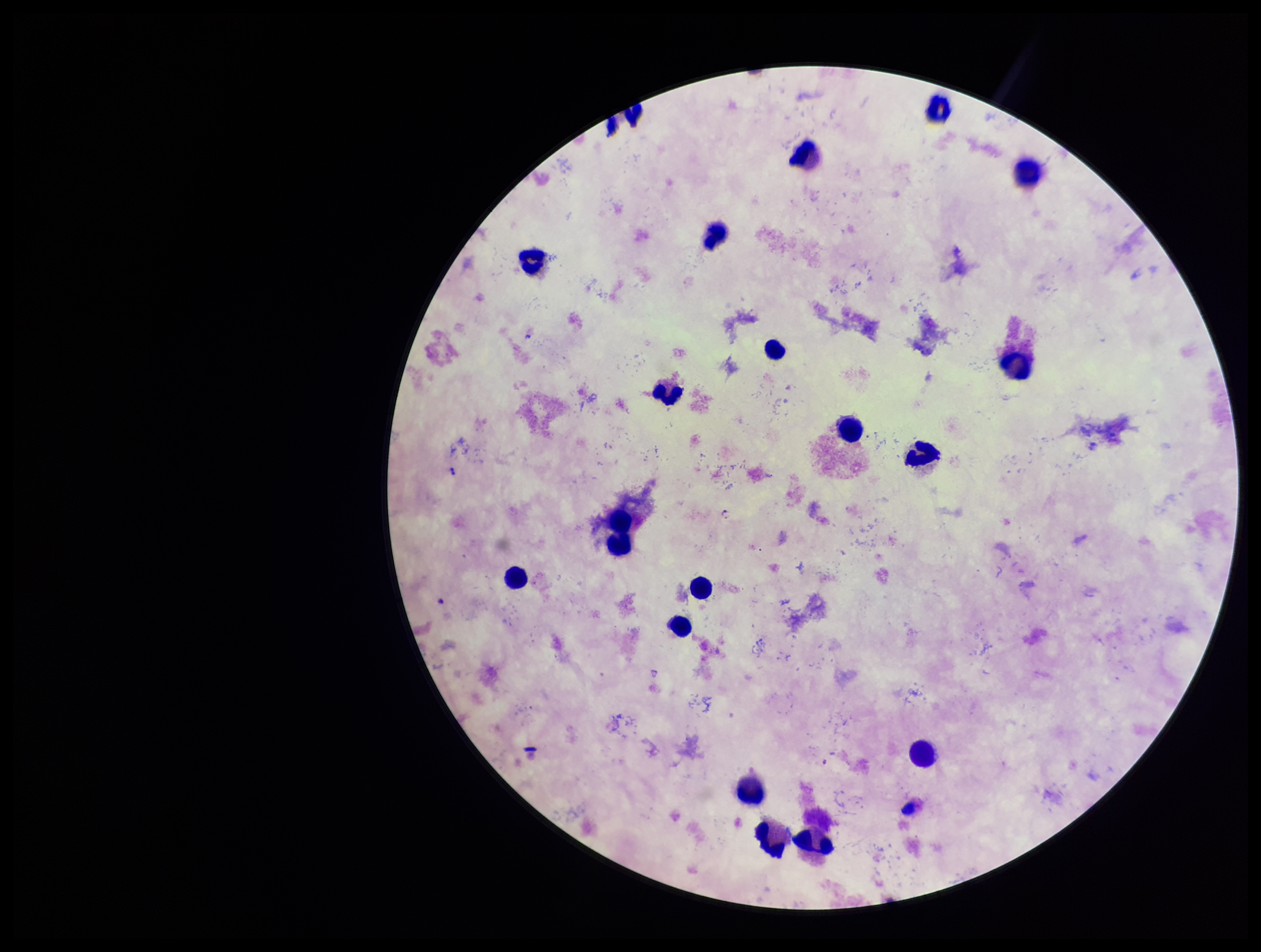 Smartphone photograph taken through the eyepiece of a microscope. Single field of view. Species reported for this patient: Plasmodium falciparum. Plasmodium parasites: none identified. Preparation: thick. Stained with Giemsa. Patient malaria status: positive. Leukocyte count: 18. Parasite count: 0. Image is 1261×952 pixels.